Describe the morphology of the erythrocytes.
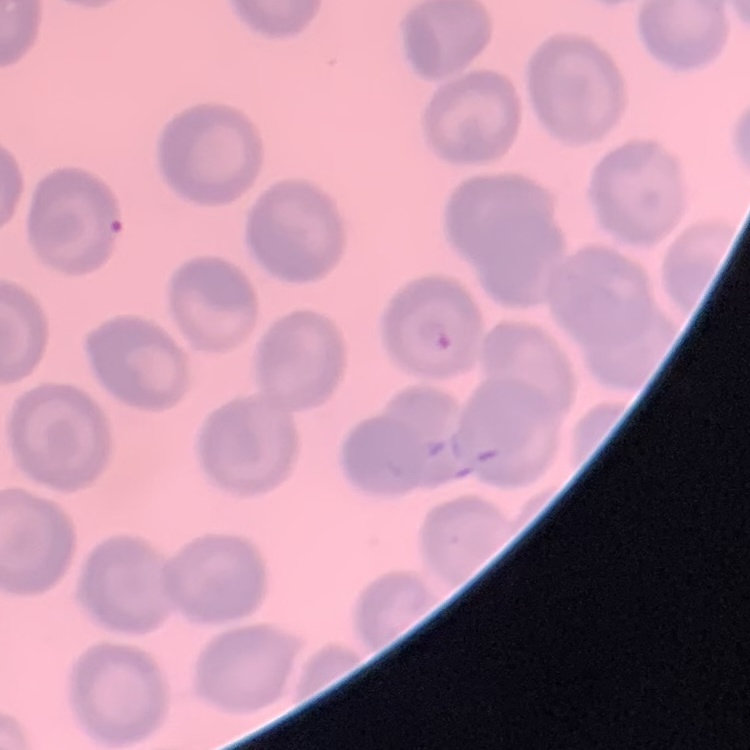

They show no rouleaux formation.

Summary:
  - Preparation: thin peripheral smear
  - Stain: Field's or Giemsa
  - Image type: square crop of a larger photomicrograph